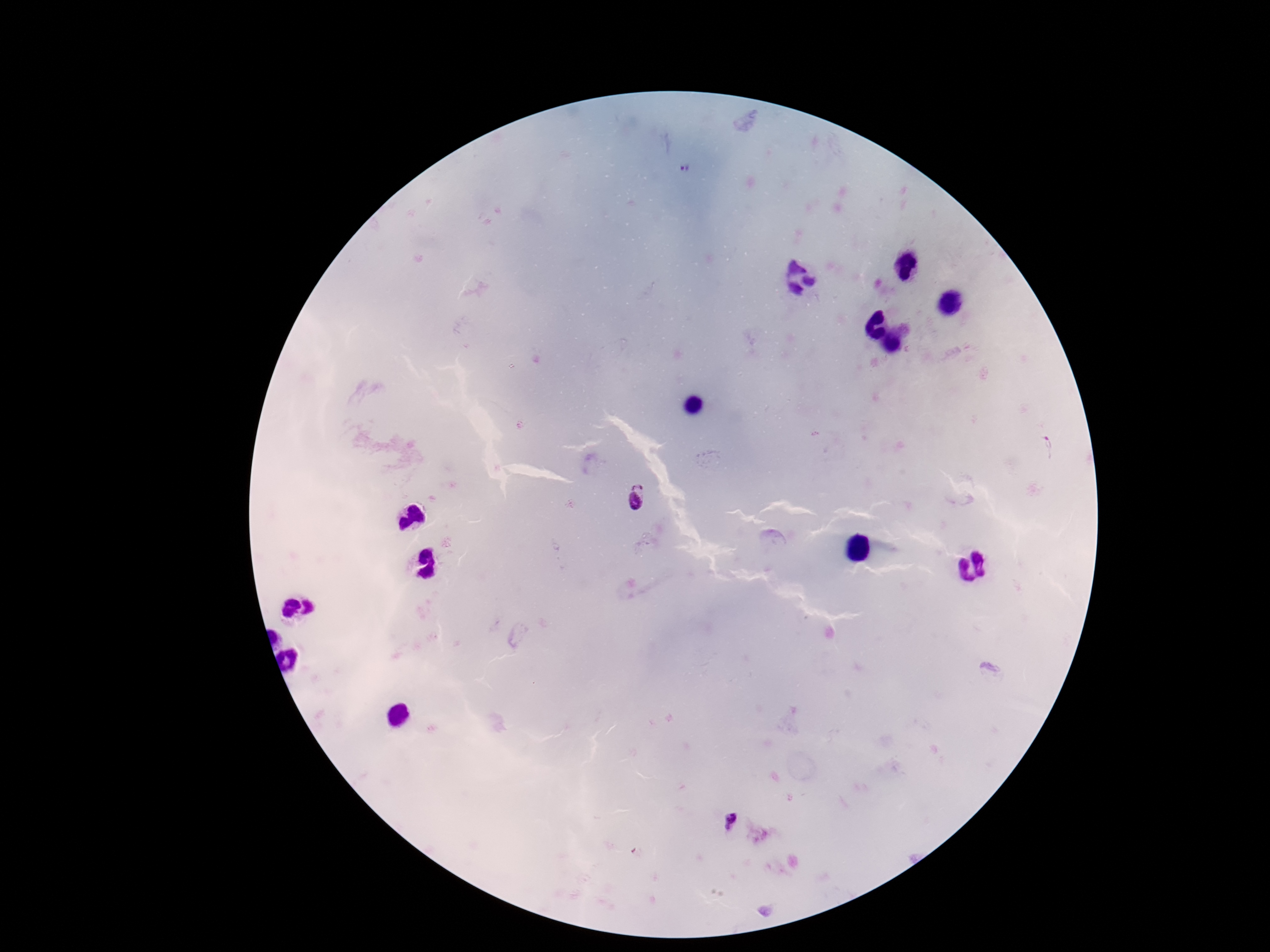
Approximate object centers, in pixels from the top-left corner.
Summary:
  - Plasmodium parasite locations: (x=686, y=167), (x=635, y=496), (x=730, y=823)
  - Stain: Giemsa
  - Capture: smartphone camera through the microscope eyepiece
  - Image size: 1270×952 pixels
  - Patient malaria status: positive
  - Magnification: 100x
  - Preparation: thick blood smear
  - Field of view: one from this slide